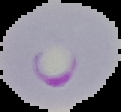 From a thin blood film. Malaria status: parasitized. Image is 121×112 pixels. Cell region segmented out of the field of view; the surrounding area is masked to black.